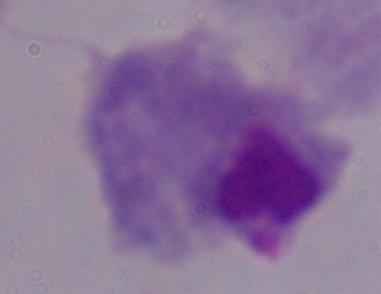
Summary:
  - Magnification: 1000x
  - Identification: trichomonad
  - Modality: photomicrograph